Classify this cell by malaria status.
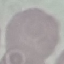

It is uninfected.

image type = automatically extracted cell patch, resized to 64 × 64 pixels
stain = Giemsa
capture = smartphone through the microscope eyepiece
preparation = thin blood film